Name the parasite shown.
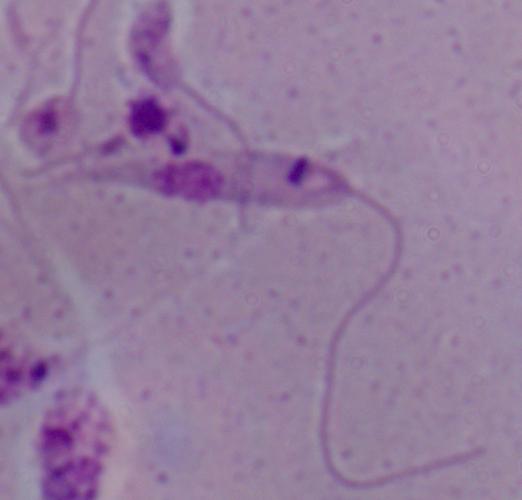

Leishmania.

modality = photomicrograph
magnification = 1000x